Give the position of every malaria parasite, noting whether each is a trophozoite, schizont, or gametocyte.
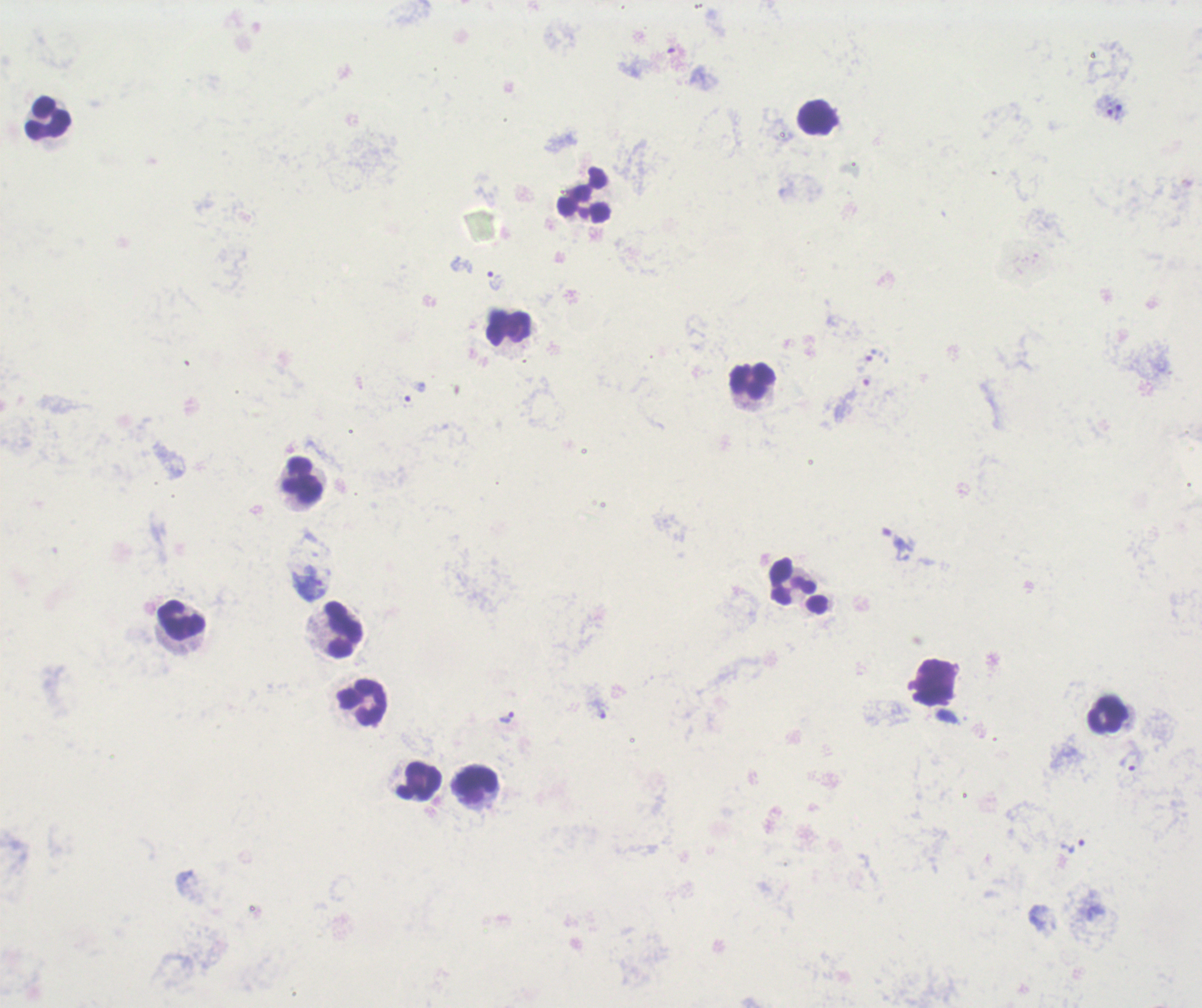
Approximate object centers, in pixels from the top-left corner.
Trophozoites: (x=1120, y=110), (x=493, y=281), (x=872, y=354), (x=406, y=402), (x=307, y=585), (x=506, y=717), (x=1129, y=759), (x=1071, y=843).
No schizont or gametocyte forms observed.

Approximate object centers, in pixels from the top-left corner.
Summary:
  - Leukocyte locations: (x=818, y=117), (x=46, y=118), (x=584, y=194), (x=508, y=328), (x=751, y=380), (x=301, y=482), (x=790, y=581), (x=182, y=621), (x=342, y=629), (x=363, y=704), (x=1106, y=716), (x=419, y=783), (x=476, y=785)
  - Background quality: unsatisfactory
  - Magnification: 100x
  - Stain: Romanowsky
  - Field of view: one from this slide
  - Context: previously used in a real diagnosis
  - Preparation: thick blood smear
  - Image size: 1202×1008 pixels